Report the malaria status of this cell.
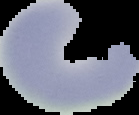
Uninfected.

Summary:
  - Preparation: thin blood smear
  - Image type: segmented cell region on a black background
  - Image size: 139×115 pixels